Report the malaria status of this cell.
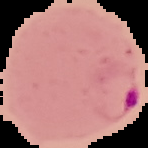

Parasitized.

Summary:
  - Image size: 148×148 pixels
  - Preparation: thin blood smear
  - Image type: segmented cell region with the area outside set to black